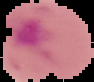

{
  "image_size": "94×82 pixels",
  "malaria_status": "parasitized",
  "image_type": "cell region segmented out of the field of view; surrounding area masked to black",
  "preparation": "thin blood film"
}